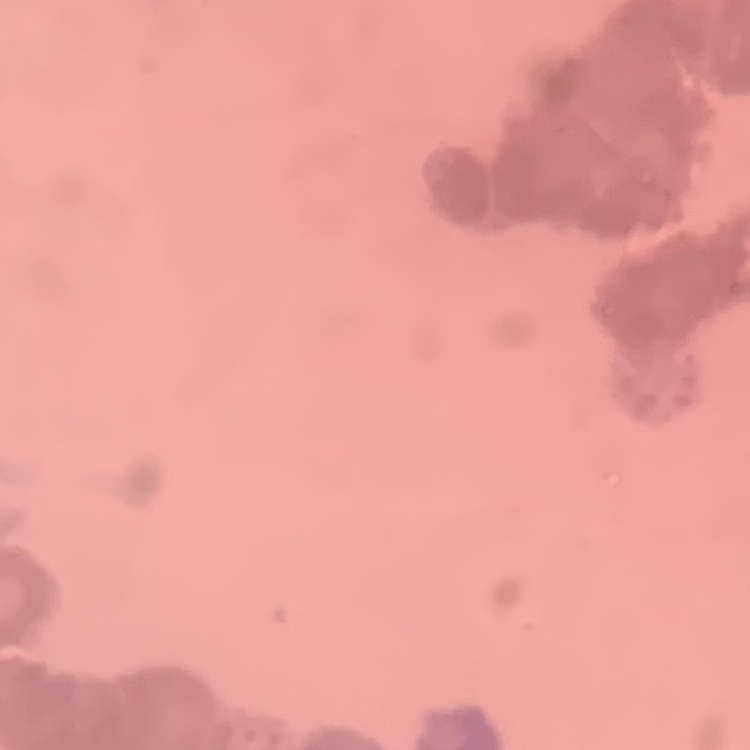 The erythrocytes exhibit rouleaux formation. One tile cut from a larger photomicrograph. Thin blood film. Stained with either Field's or Giemsa.